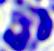
modality: photomicrograph
magnification: 400x
identification: white blood cell